Outline each blood parasite and name the species.
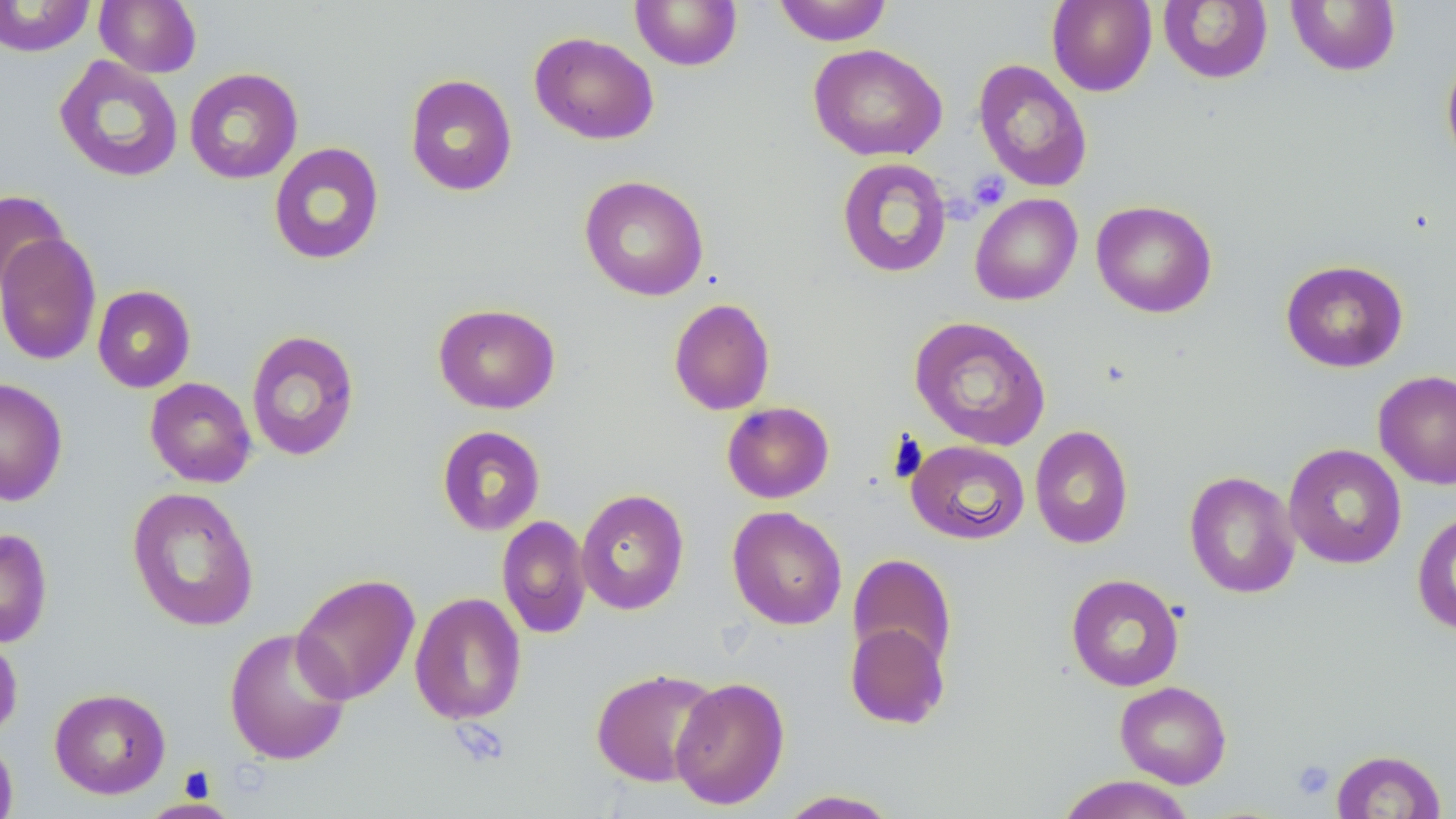
No blood parasites observed.

Summary:
  - Coordinate format: approximate bounding boxes as (x1,y1)-(x2,y2) corner pairs in pixels
  - Platelet locations: (967,170)-(1010,211), (1292,759)-(1335,800)
  - Uninfected red blood cell locations: (0,0)-(96,57), (94,0)-(202,77), (630,0)-(742,71), (774,0)-(892,46), (1047,0)-(1157,96), (1158,0)-(1273,84), (1286,1)-(1402,76), (529,31)-(659,145), (808,43)-(947,162), (1441,48)-(1456,171), (53,55)-(184,183), (973,59)-(1093,192), (183,67)-(303,184), (404,73)-(518,196), (268,142)-(385,265), (837,157)-(952,278), (579,175)-(709,301), (0,189)-(69,295), (970,193)-(1082,305), (1091,200)-(1218,318), (0,231)-(101,366), (1280,259)-(1409,372), (93,285)-(195,393), (668,298)-(775,415), (433,303)-(561,414), (908,315)-(1052,451), (245,330)-(361,461), (1373,370)-(1456,491), (145,377)-(257,488), (0,378)-(68,506), (721,401)-(834,503), (436,425)-(546,536), (1030,425)-(1133,549), (906,439)-(1030,545), (1284,443)-(1406,569), (1185,470)-(1300,599), (127,486)-(260,632), (576,488)-(689,615), (727,506)-(848,630), (1412,510)-(1456,635), (497,515)-(592,639), (0,527)-(53,648), (847,553)-(958,672), (291,573)-(420,705), (1066,574)-(1184,691), (409,592)-(527,725), (845,621)-(950,730), (224,627)-(352,766), (0,632)-(22,741), (590,667)-(720,787), (670,676)-(790,809), (1115,680)-(1232,788), (49,687)-(171,798), (0,735)-(19,819), (1331,749)-(1447,819), (1055,774)-(1197,818), (776,789)-(901,818), (140,797)-(241,819)
  - Slide-level diagnosis: no evidence of blood parasites
  - Preparation: thin blood film
  - Modality: light microscopy
  - Magnification: 1000x
  - Field of view: one of a larger specimen
  - Stain: May-Grünwald-Giemsa
  - Image size: 1456×819 pixels